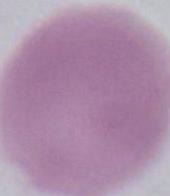

1000x magnification. An erythrocyte is shown. Micrograph.